Assess this cell for malaria.
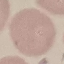
Uninfected.

Summary:
  - Capture: smartphone camera at the microscope eyepiece
  - Preparation: thin blood film
  - Image type: cell patch, automatically extracted from a larger field of view and resized to 64 × 64 pixels
  - Stain: Giemsa